State which parasite is depicted.
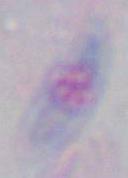

Toxoplasma gondii.

Summary:
  - Modality: micrograph
  - Magnification: 1000x